Classify this cell by malaria status.
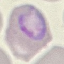
Parasitized.

Photographed with a smartphone camera at the microscope eyepiece. Giemsa-stained preparation. Automatically extracted cell patch, resized to 64 × 64 pixels. Thin smear of blood.